Describe the morphology of the red blood cells.
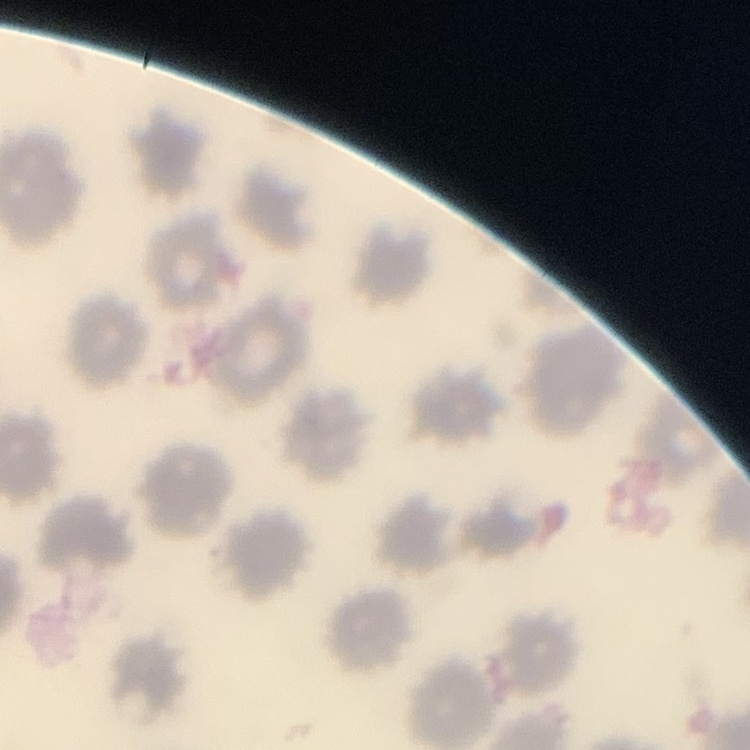

No rouleaux formation.

Thin blood film. One tile cut from a larger photomicrograph. Stained with either Field's or Giemsa.